Identify the cell.
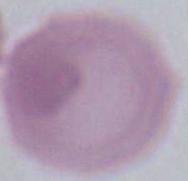
An erythrocyte.

Summary:
  - Modality: photomicrograph
  - Magnification: 1000x